Mark where leukocytes are.
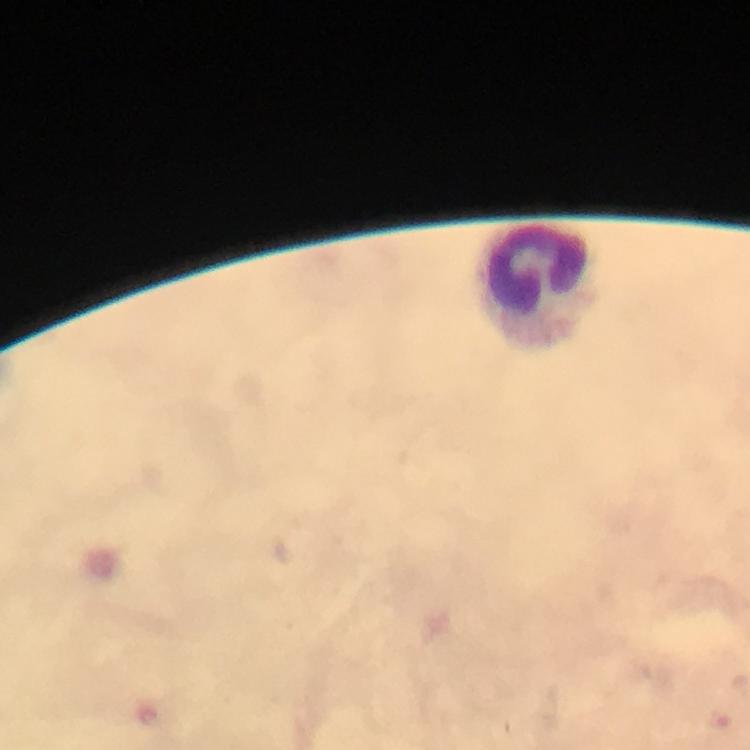
Approximate centers as [x, y] in pixels.
Leukocytes: [538, 287].

{
  "immersion_oil": "applied",
  "malaria_parasites": "none detected",
  "magnification": "100x",
  "context": "from a diagnostic examination for malaria",
  "image_size": "750×750 pixels",
  "preparation": "thick blood smear",
  "cropped_from": "a single field of view",
  "stain": "Giemsa",
  "capture": "smartphone mounted on the microscope"
}